Comment on the morphology of the erythrocytes.
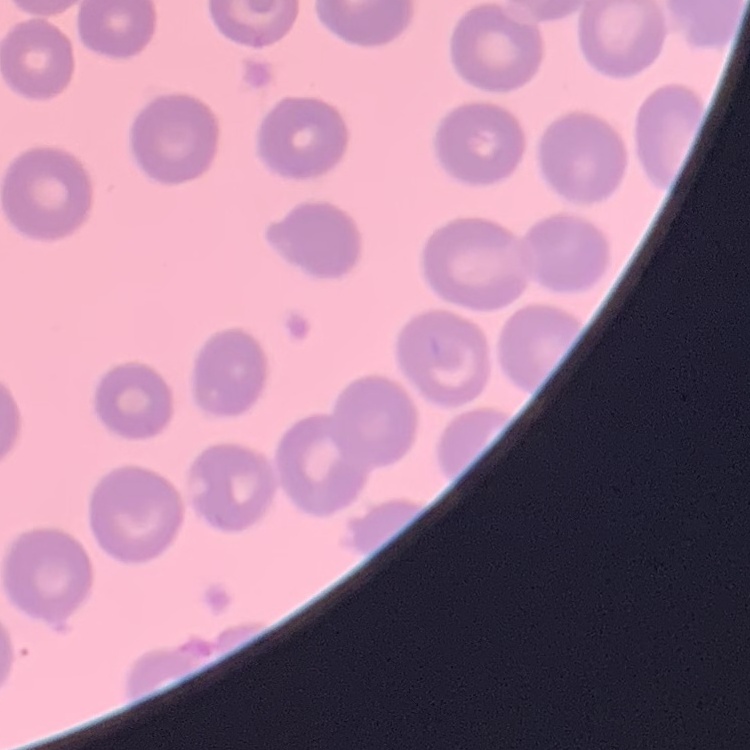
No rouleaux formation.

Thin blood smear. Stained with either Field's or Giemsa. Square crop of a larger photomicrograph.